Point out each Plasmodium parasite.
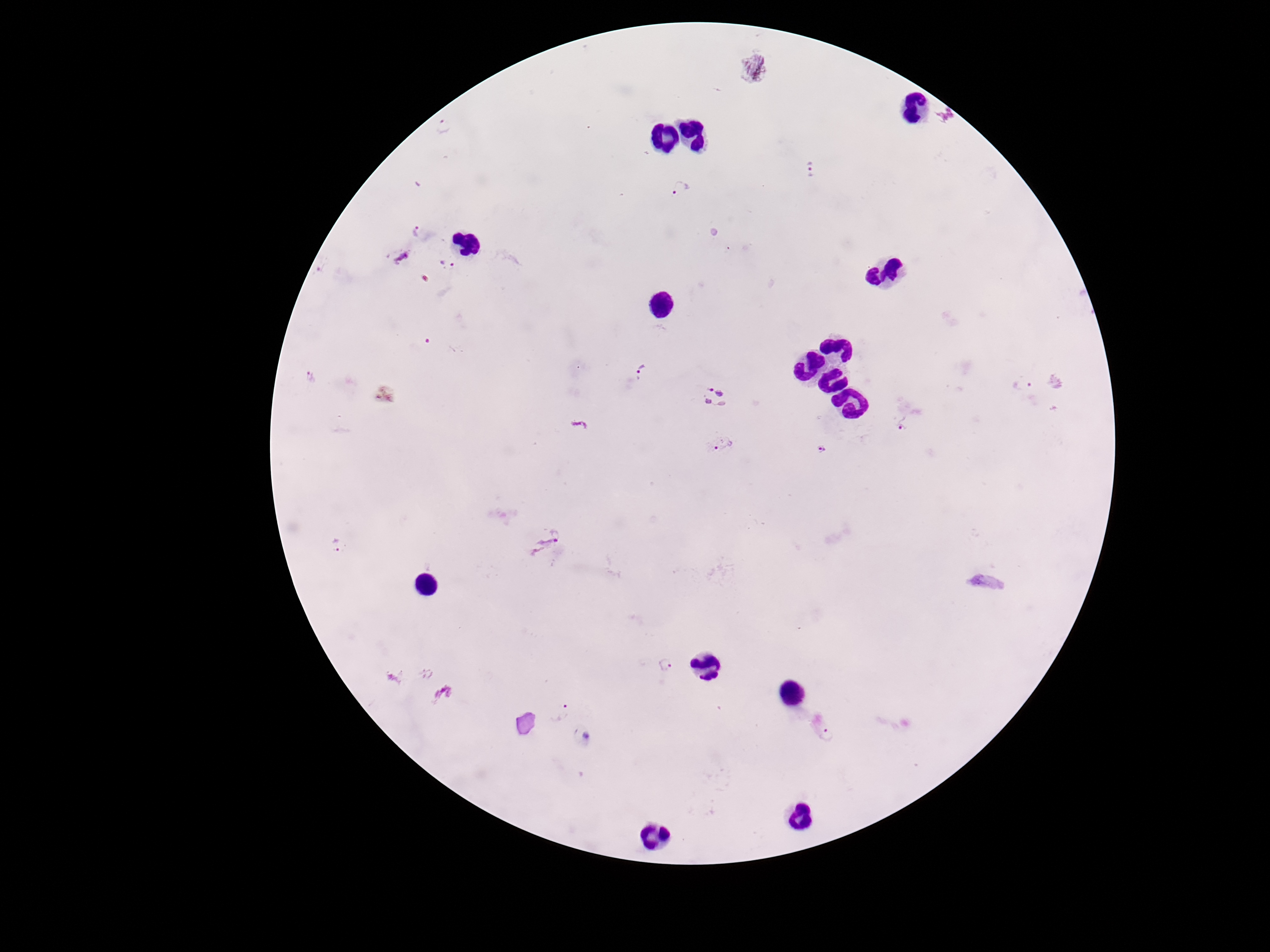

Approximate centers as (x, y) in pixels.
Plasmodium parasites: (943, 117), (444, 128), (812, 170), (681, 189), (417, 230), (399, 255), (448, 264), (643, 372), (309, 378), (1024, 385), (715, 397), (903, 424), (721, 444), (823, 450), (338, 546), (548, 546), (665, 665), (560, 709), (829, 736), (586, 739).

Patient malaria status: infected. Smartphone photograph taken through the microscope eyepiece. Image is 1270×952 pixels. 100x magnification. Thick peripheral-blood smear. Single field of view. Giemsa-stained preparation.